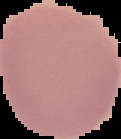

The area outside the segmented cell region is set to black. Result: no Plasmodium parasites seen. Image is 121×139 pixels. From a thin blood smear.